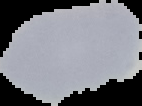
Summary:
  - Preparation: thin blood smear
  - Image type: cell region segmented out of the field of view; surrounding area masked to black
  - Image size: 142×106 pixels
  - Result: negative for Plasmodium parasites